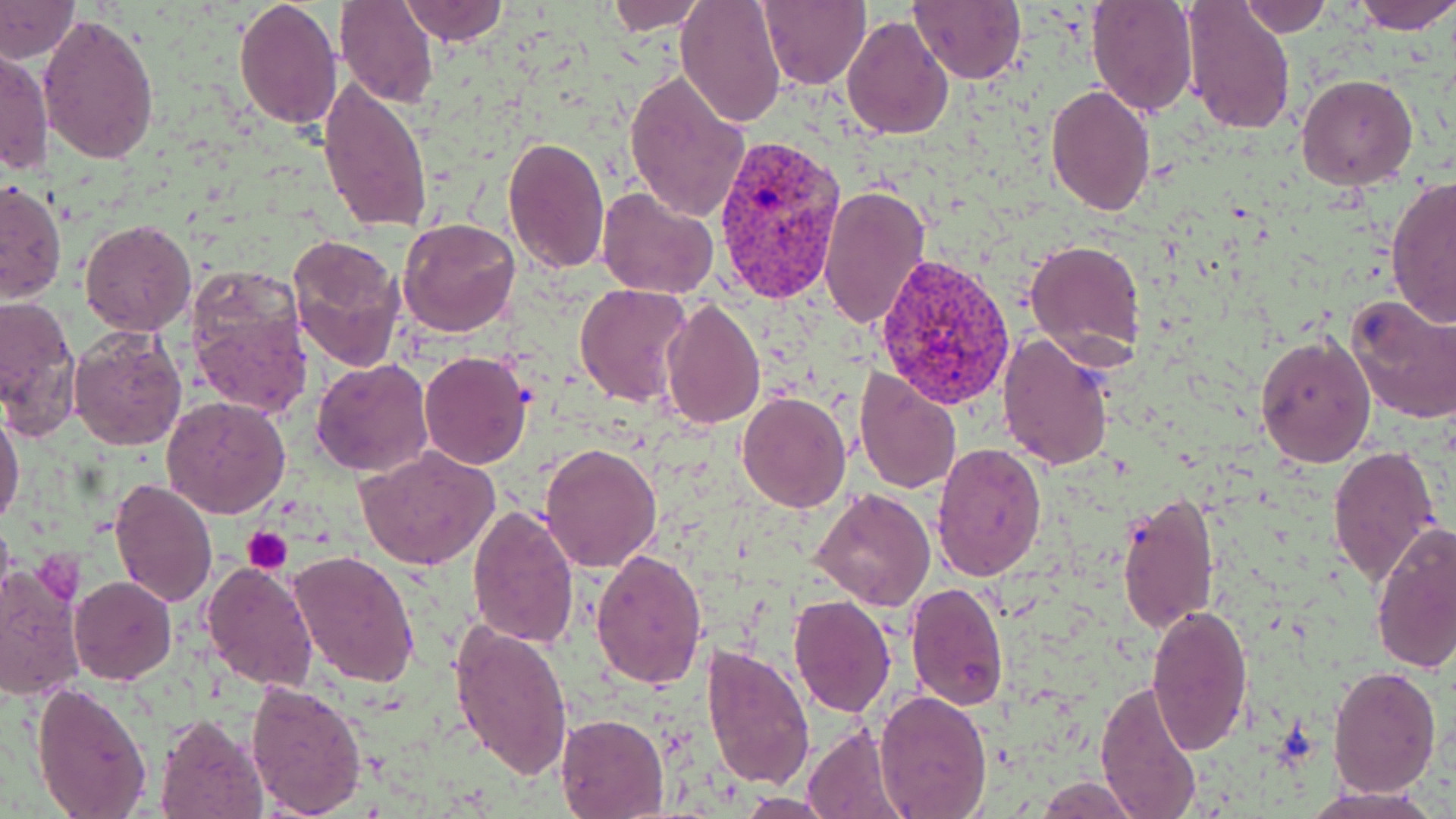

Summary:
  - Coordinate format: approximate bounding boxes as (x1,y1)-(x2,y2) corner pairs in pixels
  - Uninfected red blood cell locations: (336,0)-(438,107), (398,0)-(507,46), (604,0)-(706,33), (675,0)-(788,127), (757,0)-(870,90), (1086,0)-(1198,117), (1235,0)-(1332,37), (1350,0)-(1456,34), (233,1)-(343,132), (0,2)-(80,62), (909,2)-(1026,84), (1180,2)-(1296,134), (39,13)-(161,165), (841,15)-(953,139), (1,46)-(51,180), (623,69)-(750,224), (1295,73)-(1419,189), (317,76)-(433,233), (1045,83)-(1156,216), (501,135)-(610,274), (1384,177)-(1456,328), (1,178)-(66,305), (819,183)-(928,331), (596,186)-(718,300), (397,217)-(522,338), (79,218)-(198,336), (286,233)-(406,370), (1025,239)-(1145,360), (186,264)-(315,421), (575,284)-(690,408), (0,293)-(82,439), (1343,294)-(1456,425), (659,295)-(767,431), (68,327)-(187,451), (997,332)-(1115,472), (1255,332)-(1377,466), (419,351)-(533,467), (311,359)-(434,477), (852,368)-(961,494), (738,392)-(851,512), (162,396)-(292,519), (0,404)-(25,528), (540,442)-(663,573), (931,442)-(1047,580), (1326,446)-(1444,587), (357,448)-(500,571), (107,477)-(218,609), (809,487)-(935,611), (1117,489)-(1221,635), (468,505)-(579,650), (1369,522)-(1455,675), (288,549)-(422,688), (590,550)-(708,689), (202,559)-(318,693), (0,564)-(85,700), (70,576)-(178,685), (906,582)-(1007,714), (788,593)-(896,716), (1145,601)-(1255,755), (450,621)-(574,781), (701,646)-(815,788), (1329,664)-(1442,797), (245,678)-(367,817), (1094,679)-(1205,817), (30,682)-(153,818), (874,690)-(991,817), (555,713)-(668,817), (154,715)-(268,819), (802,724)-(907,819), (1038,777)-(1137,816), (1303,786)-(1441,819), (737,794)-(837,816)
  - Platelet locations: (242,527)-(293,575)
  - Plasmodium vivax-infected red blood cell locations: (715,134)-(844,304), (873,252)-(1017,409)
  - Slide-level diagnosis: Plasmodium vivax
  - Preparation: thin blood smear
  - Field of view: single
  - Image size: 1456×819 pixels
  - Magnification: 1000x
  - Modality: optical microscopy
  - Stain: May-Grünwald-Giemsa